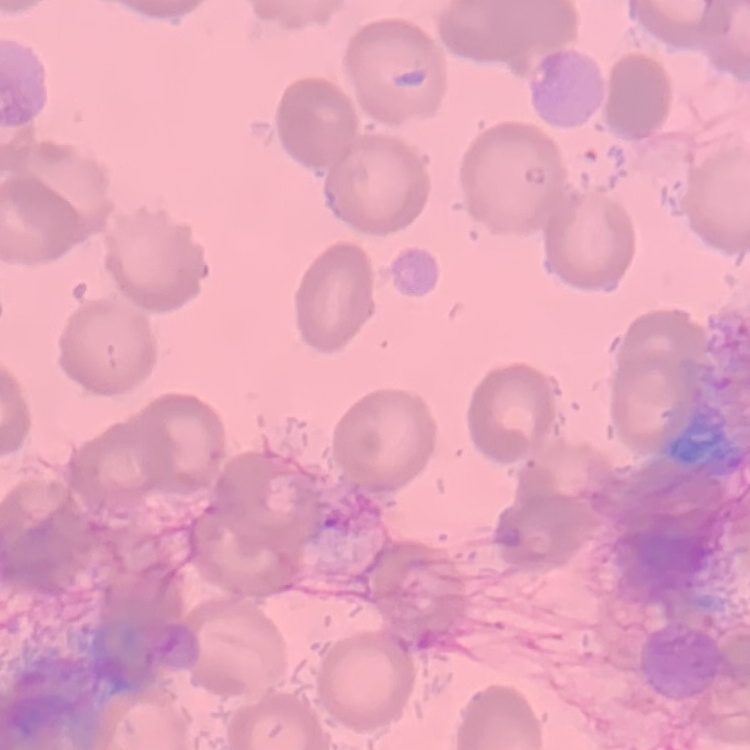
red blood cell morphology = no rouleaux formation
stain = Field's or Giemsa
image type = one tile cut from a larger photomicrograph
preparation = thin blood smear